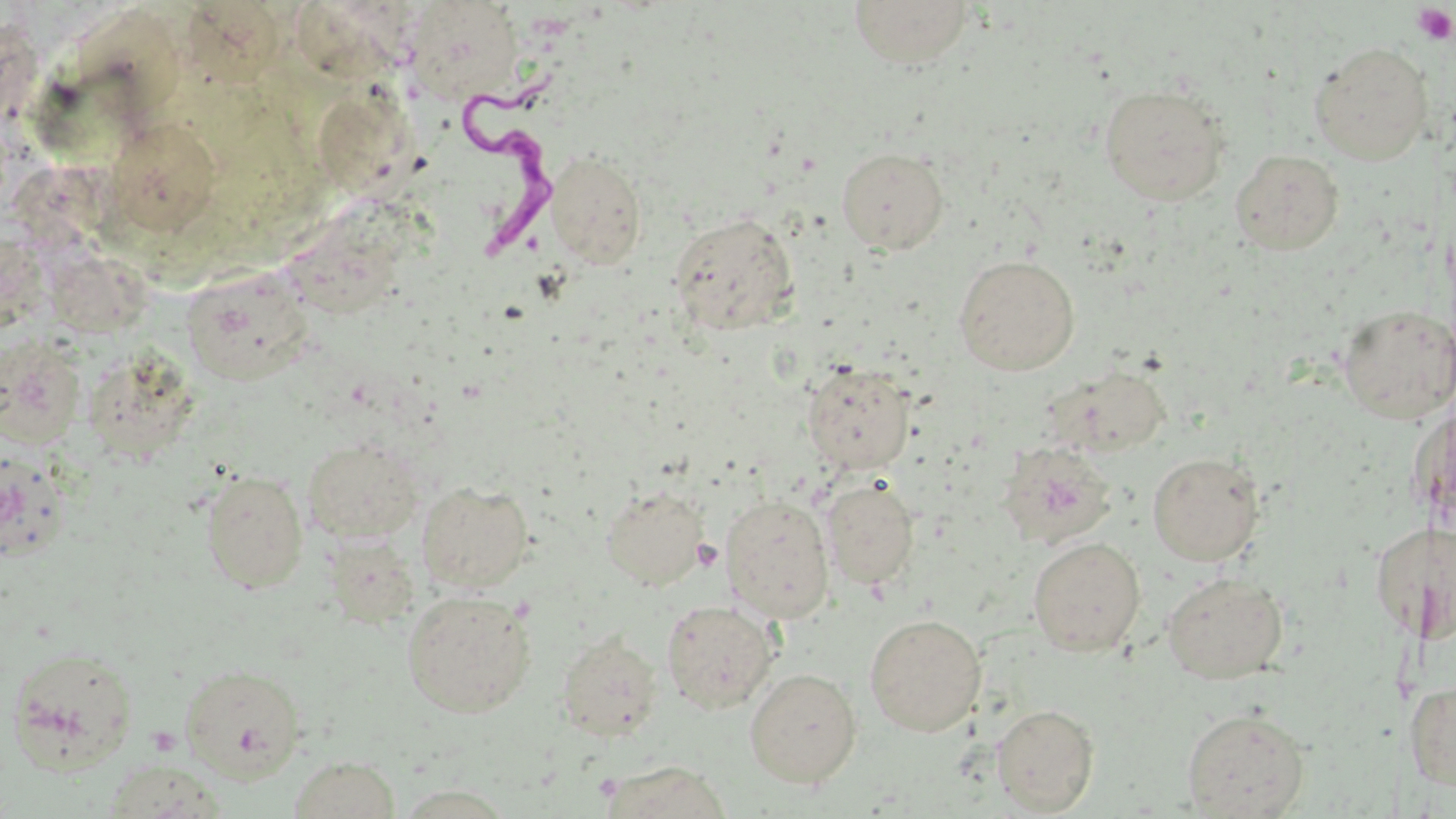
slide-level diagnosis = Trypanosoma brucei
field of view = single
stain = May-Grünwald-Giemsa
image size = 1456×819 pixels
platelet locations = approximate bounding boxes as named x1/y1/x2/y2 corners in pixels: (x1=1411, y1=3, x2=1455, y2=46)
magnification = 1000x
uninfected red blood cell locations = approximate bounding boxes as named x1/y1/x2/y2 corners in pixels: (x1=847, y1=0, x2=975, y2=69), (x1=402, y1=1, x2=524, y2=104), (x1=186, y1=7, x2=294, y2=90), (x1=1309, y1=41, x2=1433, y2=165), (x1=1097, y1=84, x2=1232, y2=206), (x1=306, y1=98, x2=441, y2=222), (x1=113, y1=128, x2=224, y2=245), (x1=837, y1=147, x2=949, y2=255), (x1=1230, y1=148, x2=1344, y2=254), (x1=545, y1=150, x2=647, y2=268), (x1=669, y1=212, x2=801, y2=336), (x1=953, y1=254, x2=1080, y2=375), (x1=48, y1=263, x2=162, y2=341), (x1=182, y1=269, x2=317, y2=388), (x1=1337, y1=304, x2=1455, y2=424), (x1=0, y1=333, x2=88, y2=449), (x1=88, y1=352, x2=202, y2=469), (x1=801, y1=361, x2=916, y2=474), (x1=1042, y1=364, x2=1189, y2=459), (x1=301, y1=436, x2=425, y2=544), (x1=996, y1=441, x2=1118, y2=549), (x1=0, y1=447, x2=70, y2=563), (x1=1147, y1=451, x2=1265, y2=565), (x1=200, y1=469, x2=309, y2=592), (x1=822, y1=477, x2=919, y2=590), (x1=417, y1=482, x2=534, y2=593), (x1=600, y1=483, x2=708, y2=590), (x1=719, y1=494, x2=834, y2=622), (x1=1424, y1=517, x2=1456, y2=648), (x1=1368, y1=519, x2=1435, y2=645), (x1=326, y1=534, x2=432, y2=645), (x1=1028, y1=536, x2=1146, y2=657), (x1=1161, y1=572, x2=1288, y2=684), (x1=402, y1=590, x2=536, y2=718), (x1=661, y1=599, x2=779, y2=714), (x1=864, y1=613, x2=987, y2=736), (x1=556, y1=632, x2=663, y2=741), (x1=4, y1=645, x2=140, y2=773), (x1=180, y1=664, x2=307, y2=782), (x1=744, y1=667, x2=862, y2=788), (x1=1404, y1=681, x2=1456, y2=792), (x1=991, y1=703, x2=1100, y2=815), (x1=1181, y1=708, x2=1310, y2=818), (x1=288, y1=755, x2=402, y2=819), (x1=101, y1=760, x2=232, y2=817), (x1=597, y1=761, x2=733, y2=817), (x1=393, y1=785, x2=517, y2=818)
Trypanosoma brucei locations = approximate bounding boxes as named x1/y1/x2/y2 corners in pixels: (x1=462, y1=73, x2=568, y2=255)
modality = optical microscopy
preparation = thin blood smear